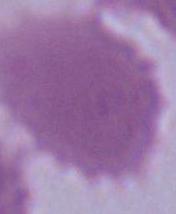

modality = photomicrograph
magnification = 1000x
identification = red blood cell